Mark where platelets are.
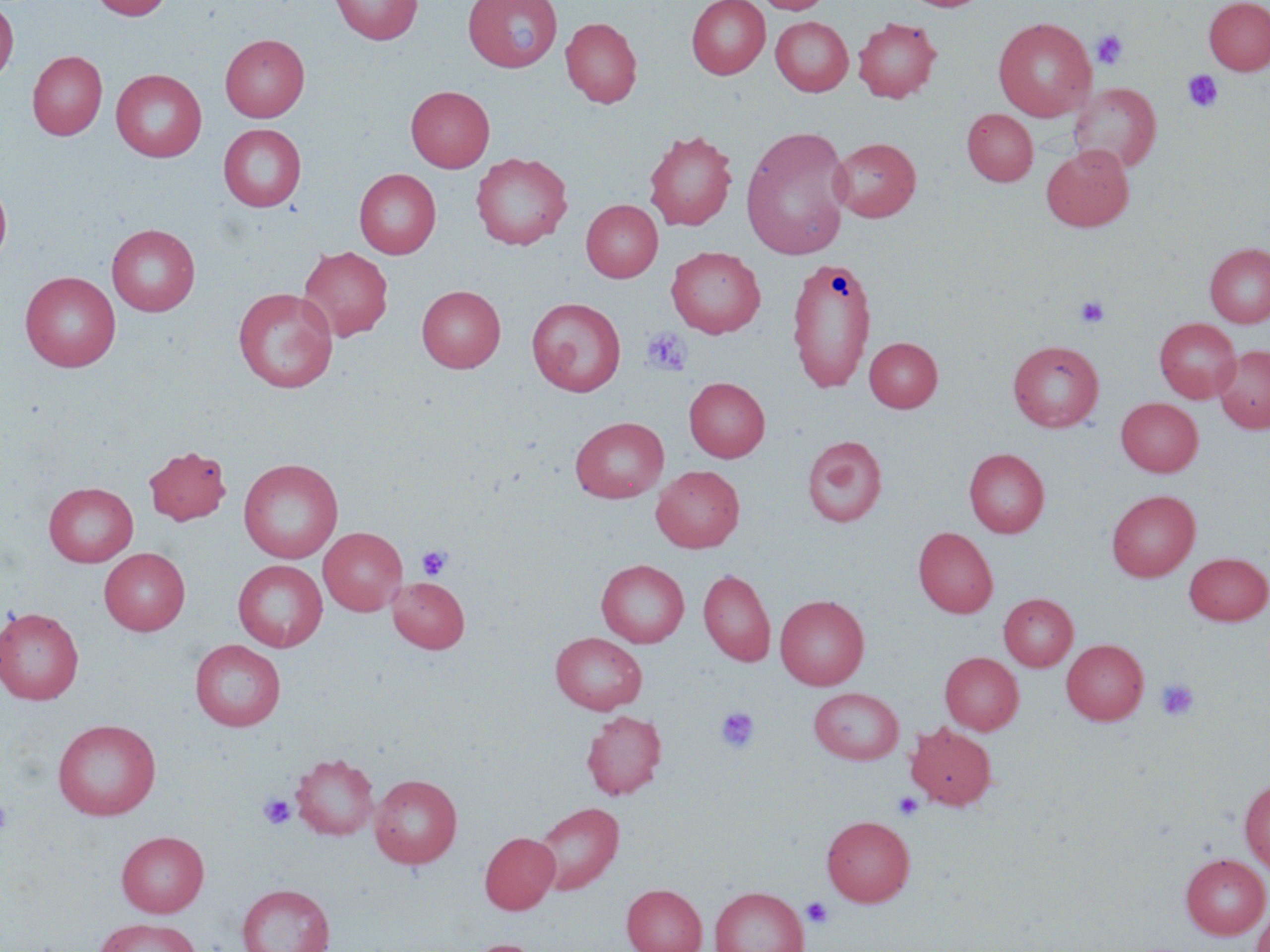
Approximate bounding boxes as (x1,y1)-(x2,y2) corner pairs in pixels.
Platelets: (1091,29)-(1129,70), (1183,70)-(1223,112), (1075,296)-(1110,328), (641,327)-(692,376), (417,546)-(452,581), (1156,678)-(1198,721), (716,706)-(760,754), (892,792)-(924,820), (258,794)-(296,830), (0,800)-(14,837), (801,896)-(834,929).

Uninfected red blood cell locations: (91,0)-(172,20), (330,0)-(423,44), (463,0)-(563,72), (686,0)-(769,80), (755,0)-(833,14), (1203,0)-(1270,75), (0,1)-(18,85), (771,16)-(853,96), (560,17)-(641,108), (853,17)-(942,102), (993,17)-(1096,121), (220,34)-(310,121), (28,50)-(107,140), (110,69)-(207,161), (1069,82)-(1161,172), (405,85)-(495,172), (963,109)-(1038,186), (218,123)-(307,211), (740,126)-(853,260), (644,129)-(737,231), (830,137)-(921,222), (1041,144)-(1134,231), (470,152)-(572,250), (354,169)-(441,258), (0,179)-(12,268), (581,200)-(663,282), (106,223)-(200,316), (1204,243)-(1270,328), (298,246)-(393,341), (666,246)-(765,337), (786,255)-(877,394), (20,271)-(121,371), (417,285)-(506,372), (233,287)-(338,392), (526,297)-(626,396), (1154,317)-(1241,403), (864,337)-(942,412), (1007,339)-(1105,432), (1214,345)-(1270,433), (684,377)-(770,462), (1116,397)-(1203,476), (570,417)-(668,502), (802,435)-(888,527), (143,445)-(231,525), (964,448)-(1049,537), (238,458)-(343,563), (651,465)-(745,552), (44,482)-(138,566), (1106,490)-(1200,581), (318,527)-(407,615), (913,527)-(997,618), (100,547)-(190,635), (1184,552)-(1269,625), (596,559)-(689,647), (232,560)-(328,651), (698,569)-(776,666), (388,576)-(470,653), (999,593)-(1077,671), (775,595)-(869,690), (0,606)-(84,705), (550,632)-(647,714), (190,639)-(285,731), (1061,639)-(1148,724), (940,652)-(1023,734), (809,687)-(904,764), (581,710)-(667,799), (52,719)-(161,820), (906,723)-(996,810), (290,753)-(379,840), (370,773)-(462,868), (1239,777)-(1270,875), (533,801)-(624,894), (821,815)-(914,906), (116,830)-(208,917), (480,831)-(560,915), (1180,853)-(1270,939), (237,883)-(334,952), (622,884)-(706,952), (710,885)-(808,952), (1250,905)-(1270,952), (93,917)-(201,952), (462,939)-(547,952). Slide-level diagnosis: no evidence of blood parasites. One field of a larger specimen. Thin blood film. Image is 1270×952 pixels. Captured at 1000x magnification. May-Grünwald-Giemsa-stained preparation. Light microscopy.